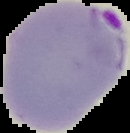
result = malaria parasites identified
preparation = thin blood smear
image size = 130×133 pixels
image type = segmented cell region on a black background